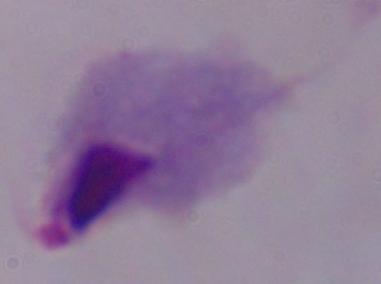
{
  "modality": "micrograph",
  "magnification": "1000x",
  "identification": "trichomonad"
}